Classify this cell by malaria status.
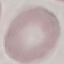

Uninfected.

Summary:
  - Stain: Giemsa
  - Image type: cell patch, automatically extracted from a larger field of view and resized to 64 × 64 pixels
  - Preparation: thin smear
  - Capture: smartphone through the microscope eyepiece